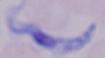
modality: micrograph
identification: trypanosome
magnification: 1000x